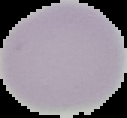 Segmented cell region on a black background. From a thin blood film. Image is 127×118 pixels. Result: no malaria parasites seen.